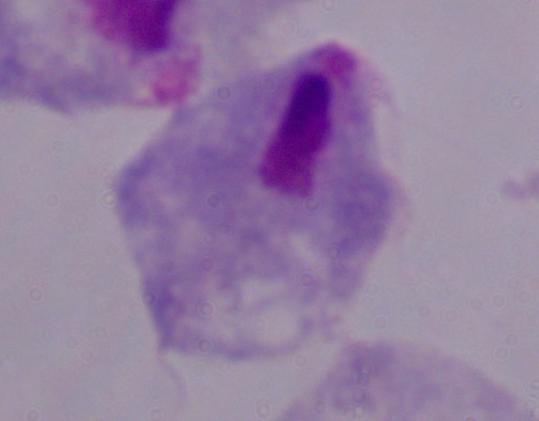 Photomicrograph. A trichomonad is shown. Captured at 1000x magnification.